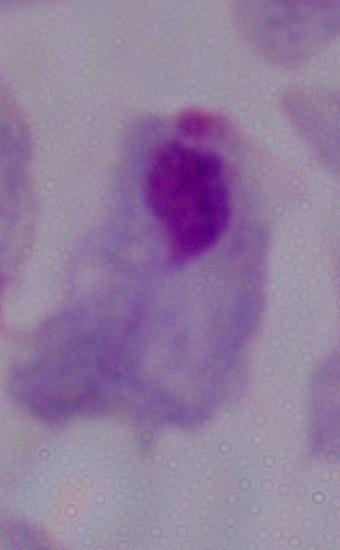

modality = photomicrograph
magnification = 1000x
identification = trichomonad